Outline each Plasmodium falciparum-infected red blood cell.
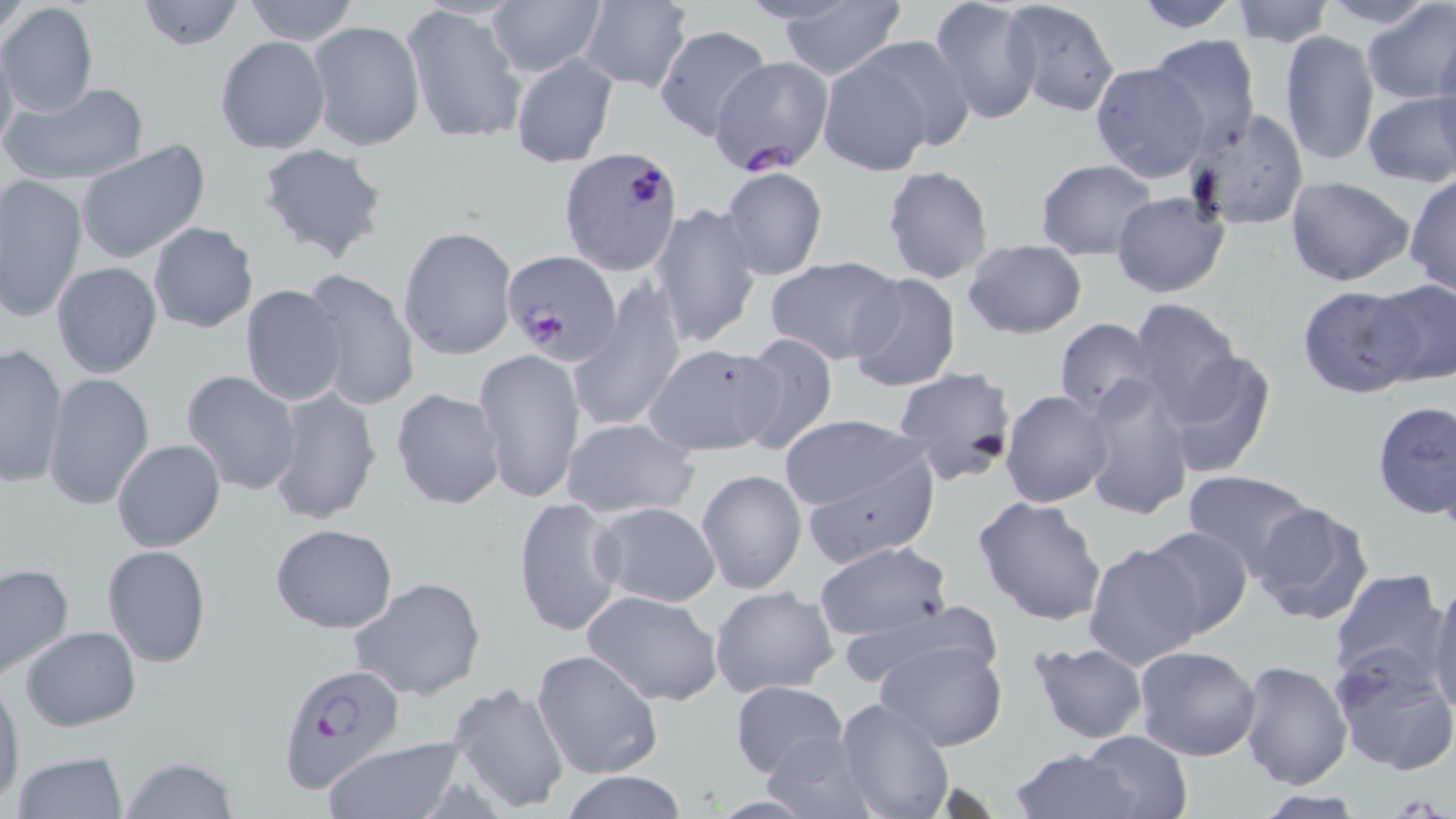

Approximate bounding boxes as (x1, y1, x2, y2) in pixels.
Plasmodium falciparum-infected red blood cells: (557, 145, 694, 275), (503, 249, 621, 365), (277, 663, 404, 795).

Uninfected red blood cell locations: (132, 0, 247, 51), (929, 0, 1045, 126), (1001, 0, 1120, 118), (1129, 0, 1247, 32), (1323, 0, 1436, 33), (1359, 0, 1456, 106), (239, 1, 362, 46), (484, 1, 606, 76), (577, 1, 693, 90), (1228, 1, 1334, 46), (0, 2, 99, 117), (774, 3, 907, 79), (404, 4, 527, 146), (307, 19, 424, 152), (654, 24, 772, 141), (1278, 30, 1380, 167), (1144, 34, 1263, 151), (1434, 34, 1456, 149), (0, 35, 19, 157), (214, 35, 330, 155), (857, 35, 979, 152), (509, 52, 619, 167), (818, 53, 939, 176), (709, 56, 831, 173), (1090, 62, 1210, 181), (1, 80, 151, 187), (1361, 91, 1456, 187), (1185, 109, 1309, 232), (76, 141, 211, 265), (255, 142, 389, 264), (1034, 158, 1160, 258), (881, 165, 994, 285), (718, 169, 828, 281), (1405, 173, 1456, 296), (0, 175, 88, 323), (1285, 175, 1415, 287), (1111, 192, 1229, 297), (19, 194, 125, 342), (649, 201, 762, 348), (146, 222, 259, 333), (399, 226, 520, 362), (962, 238, 1088, 340), (764, 257, 905, 366), (50, 262, 162, 379), (297, 269, 420, 412), (845, 272, 962, 392), (1364, 278, 1455, 388), (570, 280, 686, 434), (1296, 283, 1420, 398), (240, 285, 348, 404), (1126, 297, 1244, 417), (1052, 318, 1159, 417), (730, 333, 839, 455), (0, 343, 70, 488), (644, 343, 783, 456), (473, 347, 585, 505), (1159, 347, 1277, 478), (893, 364, 1020, 486), (180, 370, 304, 495), (44, 373, 154, 511), (1080, 377, 1196, 520), (266, 387, 383, 527), (391, 387, 507, 509), (1000, 389, 1115, 508), (1372, 400, 1456, 519), (777, 416, 929, 517), (560, 417, 699, 520), (112, 439, 226, 553), (795, 447, 940, 567), (696, 469, 807, 595), (1181, 469, 1318, 575), (973, 495, 1109, 626), (511, 496, 627, 636), (1247, 501, 1376, 628), (592, 502, 722, 606), (270, 524, 398, 632), (1137, 526, 1255, 639), (814, 540, 956, 643), (1081, 540, 1207, 669), (101, 545, 211, 667), (0, 561, 74, 679), (1326, 568, 1449, 685), (350, 575, 485, 701), (1428, 578, 1456, 716), (709, 584, 839, 697), (582, 590, 724, 707), (837, 601, 1004, 694), (21, 627, 141, 730), (871, 639, 1009, 751), (1026, 642, 1148, 745), (1132, 645, 1261, 762), (532, 647, 662, 780), (1328, 647, 1456, 778), (1237, 659, 1354, 790), (0, 676, 23, 805), (729, 680, 850, 780), (445, 681, 570, 815), (832, 698, 955, 819), (1077, 730, 1193, 818), (761, 731, 875, 818), (321, 739, 464, 819), (1005, 747, 1142, 818), (10, 750, 128, 819), (118, 756, 238, 819), (560, 770, 688, 819). Slide-level diagnosis: Plasmodium falciparum. May-Grünwald-Giemsa stain. One field of a larger specimen. 1000x magnification. Image is 1456×819 pixels. Thin blood film. Light microscopy.